Describe the morphology of the red blood cells.
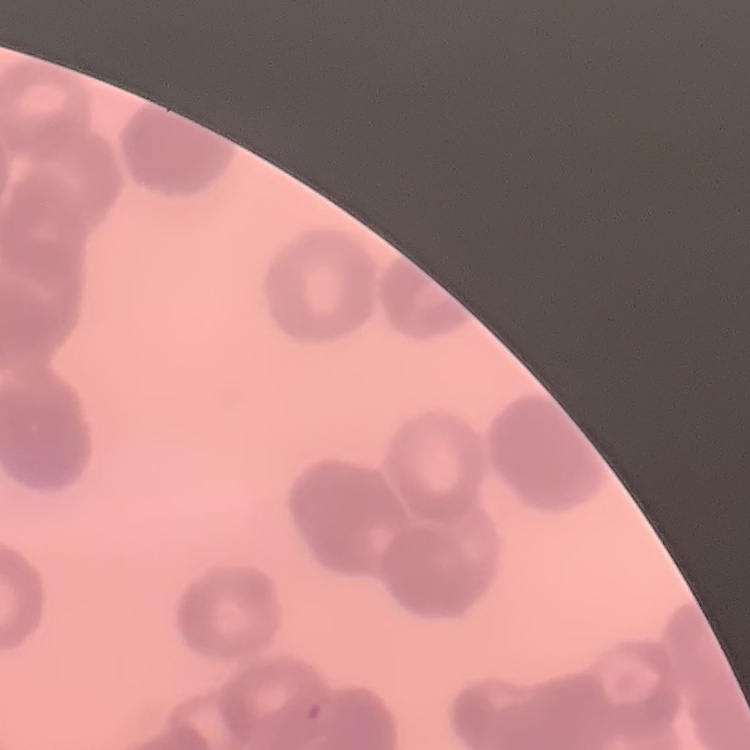

They show rouleaux formation.

Thin peripheral smear. Stained with either Field's or Giemsa. Square crop of a larger photomicrograph.